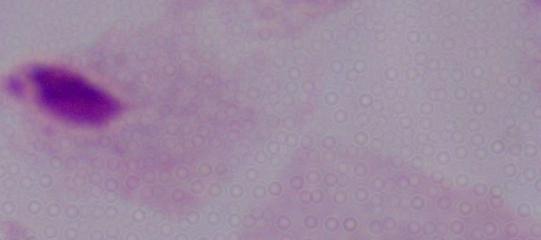 Micrograph. Captured at 1000x magnification. A trichomonad is seen.